Name the blood parasite species.
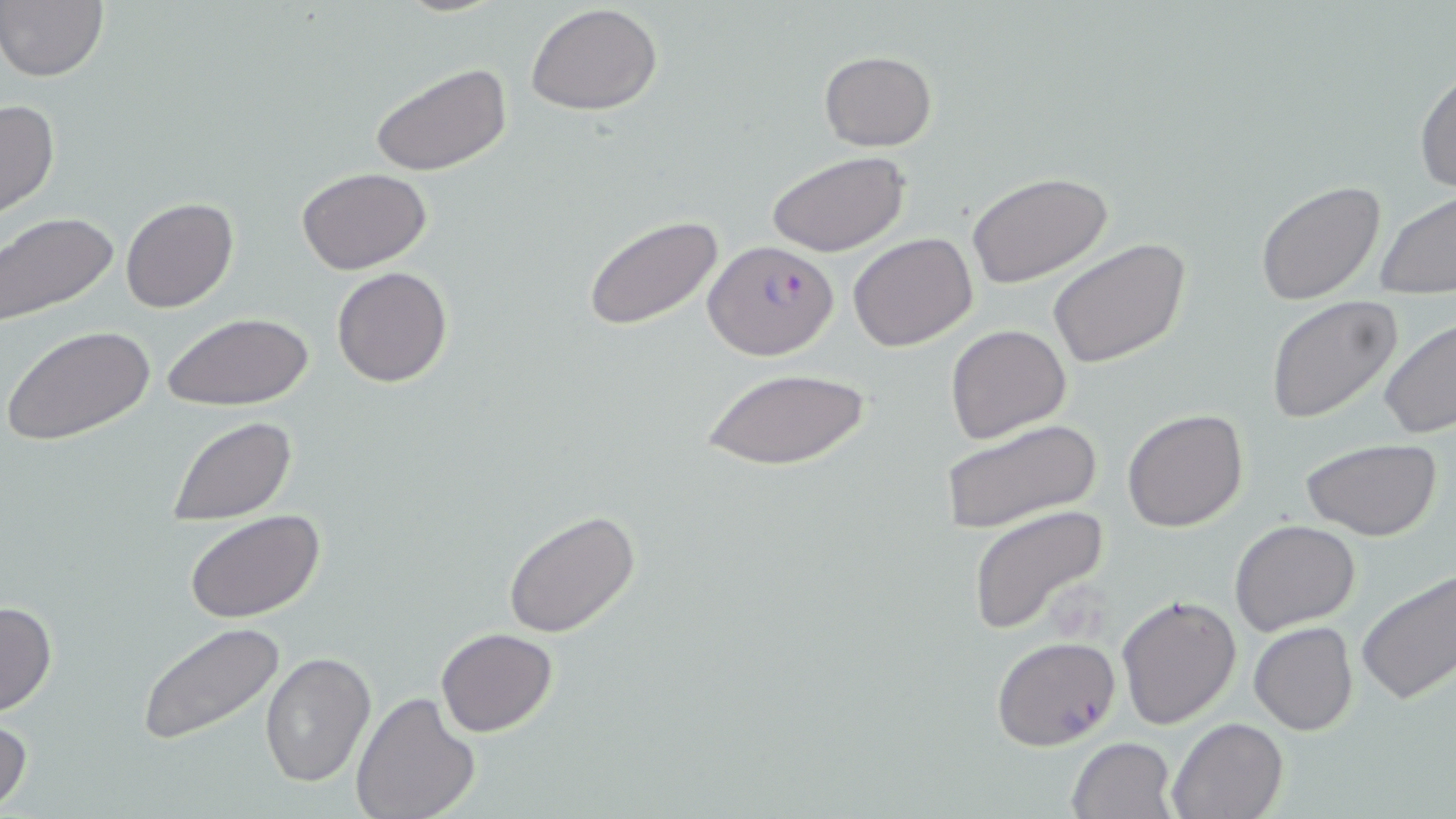

Plasmodium falciparum.

{
  "uninfected_red_blood_cell_locations": "approximate bounding boxes as named x1/y1/x2/y2 corners in pixels: (x1=1, y1=2, x2=108, y2=82), (x1=525, y1=4, x2=663, y2=115), (x1=819, y1=50, x2=936, y2=151), (x1=370, y1=62, x2=513, y2=177), (x1=1414, y1=64, x2=1456, y2=195), (x1=0, y1=98, x2=60, y2=221), (x1=767, y1=150, x2=911, y2=259), (x1=297, y1=168, x2=434, y2=276), (x1=967, y1=173, x2=1113, y2=287), (x1=1255, y1=179, x2=1386, y2=303), (x1=1375, y1=191, x2=1456, y2=298), (x1=120, y1=198, x2=237, y2=314), (x1=0, y1=211, x2=120, y2=327), (x1=583, y1=213, x2=727, y2=334), (x1=849, y1=233, x2=978, y2=352), (x1=1047, y1=239, x2=1191, y2=371), (x1=332, y1=266, x2=452, y2=388), (x1=1264, y1=296, x2=1402, y2=425), (x1=162, y1=314, x2=311, y2=412), (x1=1379, y1=318, x2=1456, y2=442), (x1=2, y1=323, x2=156, y2=447), (x1=946, y1=324, x2=1073, y2=444), (x1=700, y1=365, x2=871, y2=473), (x1=1123, y1=408, x2=1250, y2=532), (x1=167, y1=416, x2=295, y2=526), (x1=942, y1=417, x2=1101, y2=534), (x1=1301, y1=437, x2=1443, y2=541), (x1=967, y1=504, x2=1111, y2=634), (x1=185, y1=509, x2=326, y2=624), (x1=501, y1=510, x2=640, y2=638), (x1=1230, y1=519, x2=1361, y2=638), (x1=1355, y1=566, x2=1456, y2=708), (x1=1115, y1=591, x2=1240, y2=729), (x1=0, y1=599, x2=58, y2=716), (x1=138, y1=621, x2=286, y2=745), (x1=1249, y1=622, x2=1360, y2=735), (x1=436, y1=628, x2=557, y2=737), (x1=260, y1=651, x2=377, y2=790), (x1=351, y1=691, x2=480, y2=819), (x1=0, y1=715, x2=33, y2=814), (x1=1168, y1=716, x2=1289, y2=819), (x1=1066, y1=736, x2=1177, y2=819)",
  "modality": "light microscopy",
  "stain": "May-Grünwald-Giemsa",
  "field_of_view": "one of a larger specimen",
  "image_size": "1456×819 pixels",
  "preparation": "thin blood film",
  "magnification": "1000x",
  "plasmodium_falciparum_infected_red_blood_cell_locations": "approximate bounding boxes as named x1/y1/x2/y2 corners in pixels: (x1=705, y1=240, x2=840, y2=358), (x1=992, y1=636, x2=1120, y2=752)"
}